Report the malaria status of this cell.
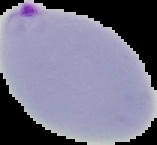
Parasitized.

Summary:
  - Preparation: thin blood smear
  - Image type: segmented cell region with the area outside set to black
  - Image size: 157×145 pixels